State which parasite is depicted.
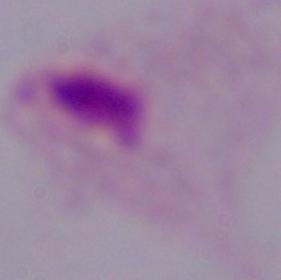
This is a trichomonad.

Photomicrograph. 1000x magnification.